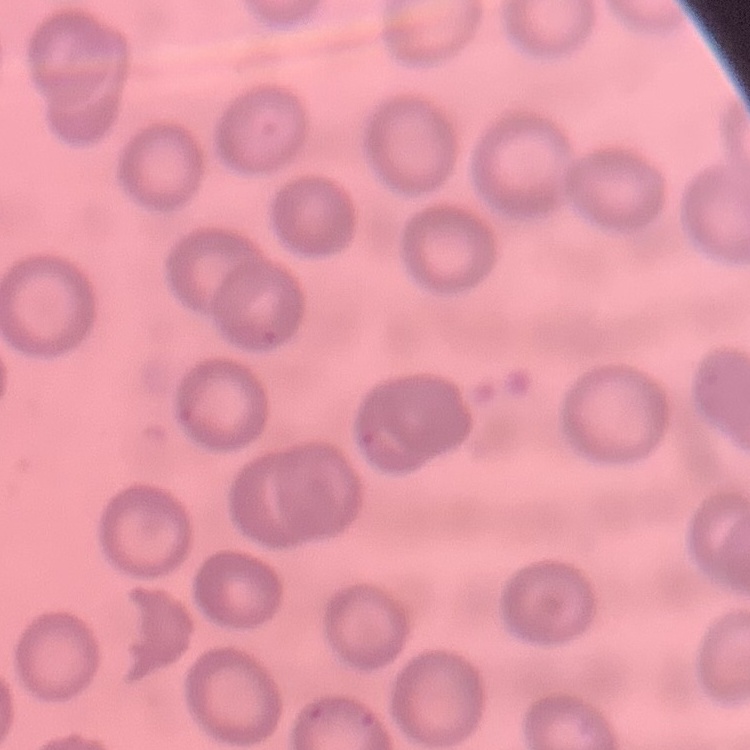 The red blood cells exhibit no rouleaux formation. Thin blood smear. One tile cut from a larger photomicrograph. Stained with either Field's or Giemsa.